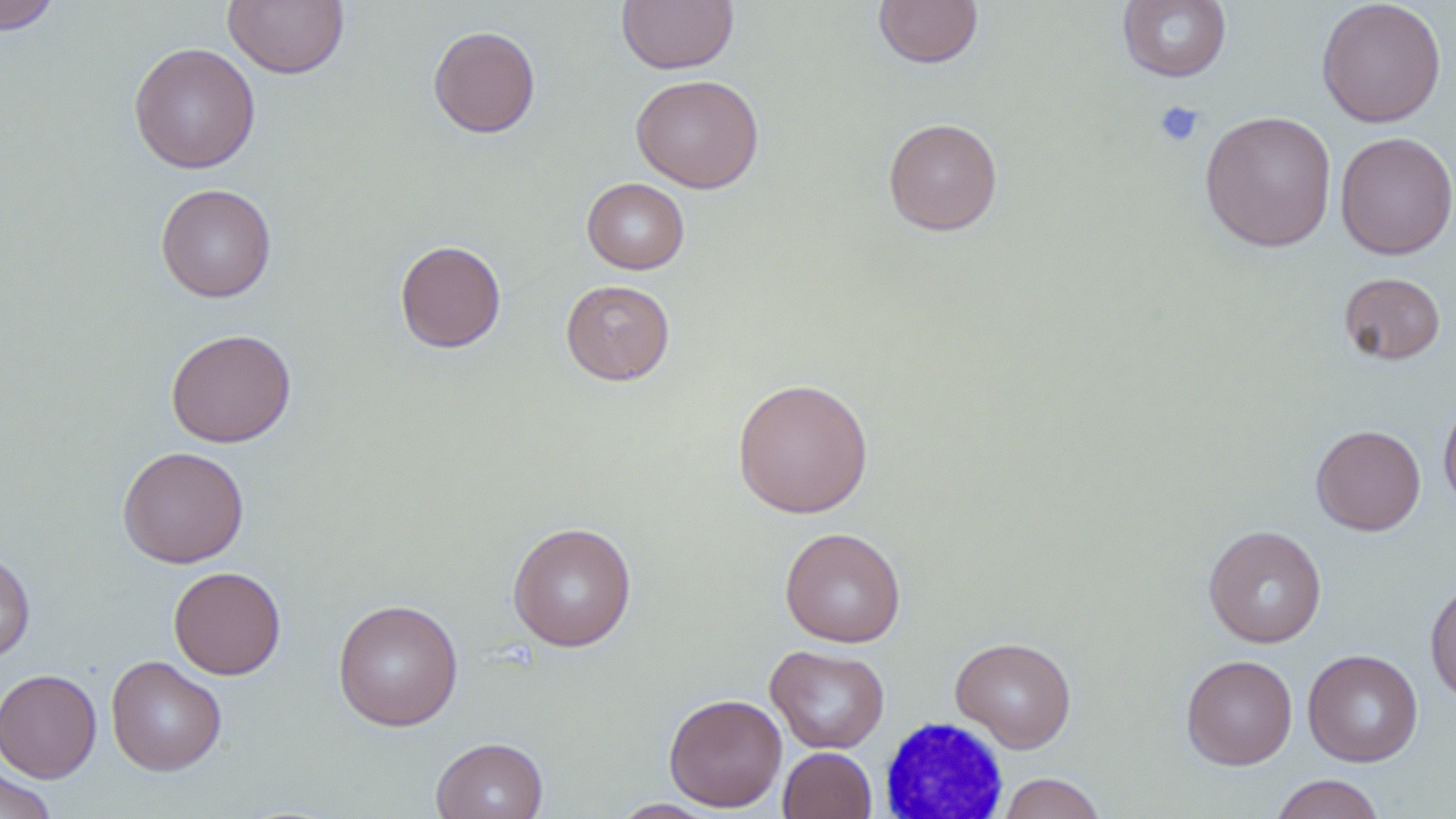

slide_level_diagnosis: no evidence of blood parasites
preparation: thin blood film
stain: May-Grünwald-Giemsa
white_blood_cell_locations: 'approximate bounding boxes as [x1, y1, x2, y2] in pixels: [879, 717, 1012, 819]'
field_of_view: single
magnification: 1000x
uninfected_red_blood_cell_locations: 'approximate bounding boxes as [x1, y1, x2, y2] in pixels: [0, 0, 59, 33], [223, 0, 350, 80], [616, 0, 739, 74], [873, 0, 983, 68], [1316, 0, 1446, 127], [1117, 1, 1232, 83], [428, 25, 540, 138], [128, 41, 261, 174], [631, 74, 764, 193], [1199, 109, 1337, 252], [883, 118, 1002, 235], [1334, 131, 1456, 260], [581, 178, 689, 274], [156, 183, 277, 303], [395, 240, 506, 353], [1338, 272, 1446, 365], [560, 279, 675, 385], [165, 328, 296, 448], [731, 377, 875, 518], [1438, 395, 1456, 511], [1311, 424, 1426, 536], [117, 446, 249, 568], [507, 521, 637, 652], [1203, 524, 1327, 648], [779, 526, 906, 648], [0, 552, 36, 662], [168, 566, 286, 680], [1425, 579, 1456, 704], [332, 598, 464, 731], [950, 636, 1077, 753], [765, 645, 890, 754], [1303, 649, 1423, 766], [1180, 654, 1297, 770], [106, 655, 227, 776], [0, 668, 101, 782], [663, 693, 788, 812], [431, 737, 548, 819], [778, 746, 877, 818], [0, 762, 58, 819], [996, 772, 1107, 819], [1269, 773, 1385, 819], [609, 798, 721, 818]'
platelet_locations: 'approximate bounding boxes as [x1, y1, x2, y2] in pixels: [1154, 100, 1205, 147]'
modality: optical microscopy
image_size: 1456×819 pixels